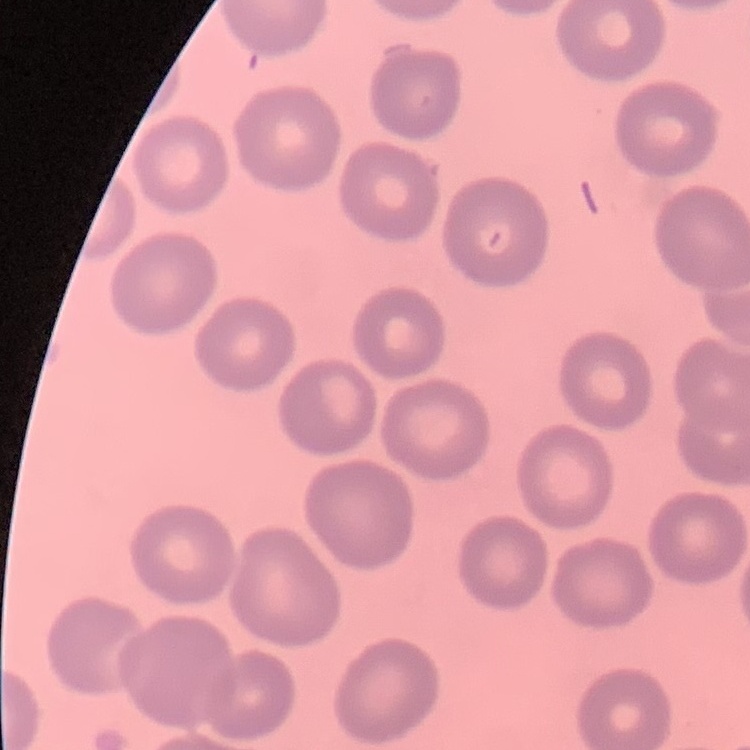
The erythrocytes show no rouleaux formation. Stained with either Field's or Giemsa. Thin blood film. Square crop of a larger photomicrograph.